Name the blood parasite species.
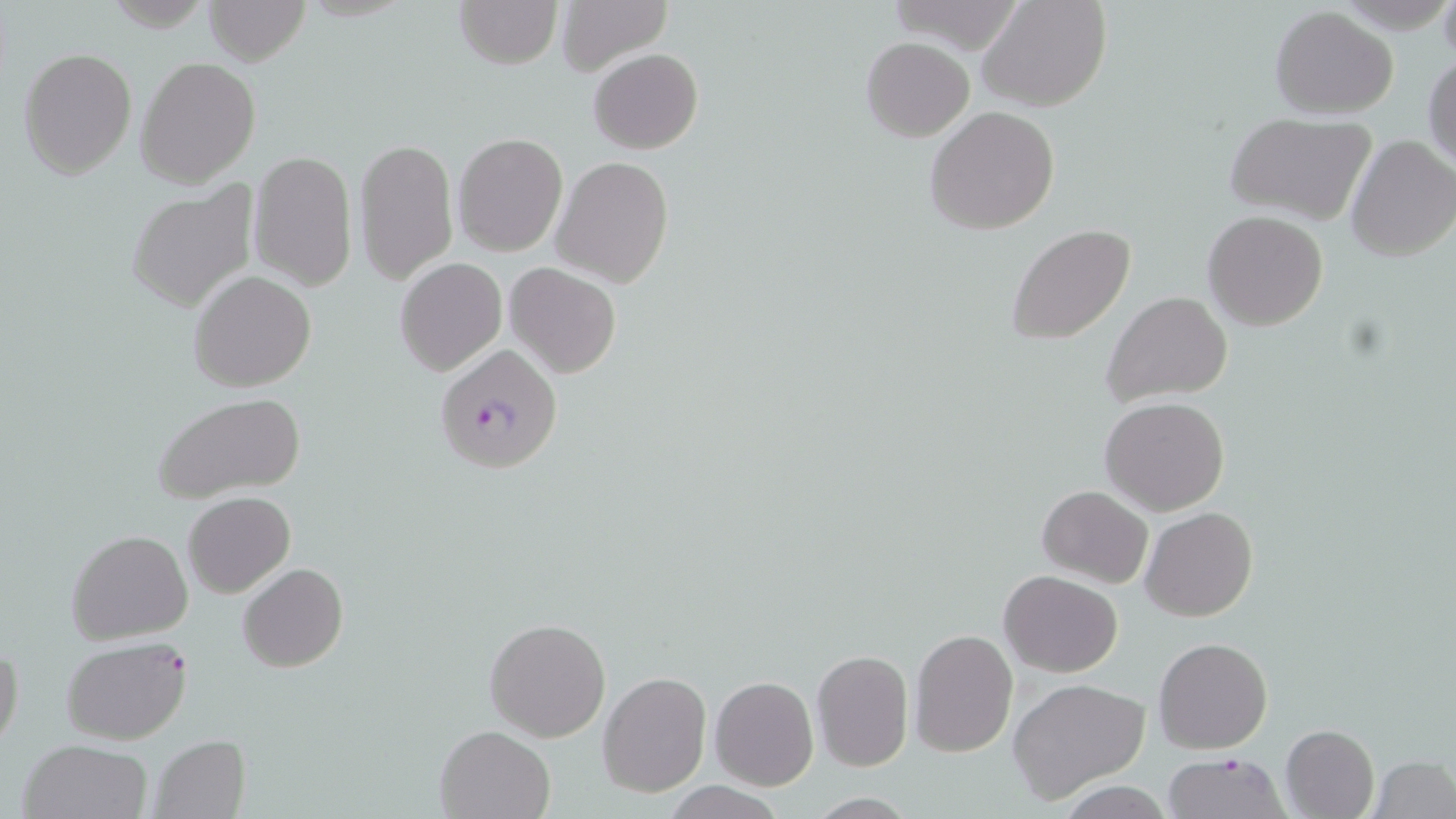

Plasmodium falciparum.

Summary:
  - Coordinate format: approximate bounding boxes as [x1, y1, x2, y2] in pixels
  - Plasmodium falciparum-infected red blood cell locations: [435, 343, 564, 477], [62, 639, 192, 745], [1162, 752, 1289, 819]
  - Uninfected red blood cell locations: [206, 0, 309, 66], [453, 0, 561, 69], [553, 0, 670, 75], [979, 0, 1111, 112], [1438, 0, 1456, 65], [1269, 6, 1398, 117], [860, 37, 974, 141], [18, 47, 137, 178], [589, 48, 702, 153], [1425, 51, 1456, 171], [136, 56, 260, 187], [924, 107, 1060, 234], [1225, 114, 1375, 225], [454, 133, 568, 256], [1345, 135, 1456, 262], [354, 136, 459, 286], [249, 148, 357, 291], [553, 156, 673, 287], [124, 180, 260, 316], [1203, 210, 1328, 330], [1006, 224, 1134, 347], [395, 257, 506, 376], [506, 262, 622, 379], [188, 271, 316, 392], [1102, 290, 1234, 409], [152, 391, 307, 502], [1100, 397, 1230, 517], [1037, 484, 1153, 588], [183, 492, 296, 599], [1141, 507, 1257, 622], [66, 529, 193, 644], [238, 564, 349, 673], [999, 571, 1123, 676], [484, 616, 612, 742], [909, 629, 1019, 759], [1154, 636, 1271, 752], [0, 642, 24, 754], [811, 650, 914, 770], [596, 672, 712, 797], [709, 677, 819, 791], [1008, 677, 1150, 803], [1281, 724, 1381, 818], [434, 726, 555, 819], [149, 734, 251, 818], [17, 738, 152, 819], [1370, 756, 1455, 819], [1054, 781, 1180, 817]
  - Preparation: thin blood film
  - Stain: May-Grünwald-Giemsa
  - Field of view: one of a larger specimen
  - Image size: 1456×819 pixels
  - Magnification: 1000x
  - Modality: optical microscopy